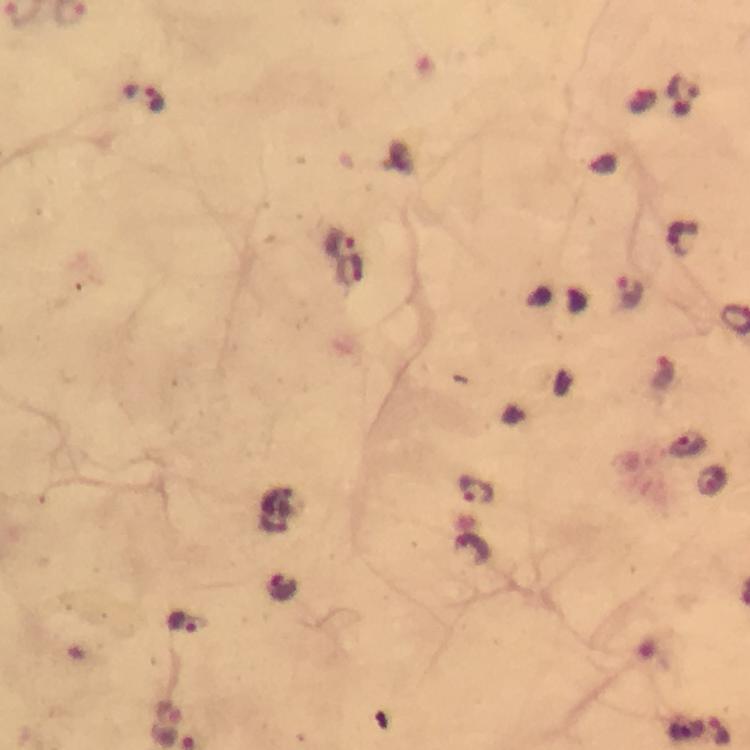 Approximate object centers, in pixels from the top-left corner. Plasmodium parasite locations: (x=141, y=100), (x=681, y=239), (x=341, y=241), (x=630, y=292), (x=664, y=373), (x=689, y=444), (x=712, y=481), (x=476, y=490), (x=475, y=547), (x=281, y=587), (x=183, y=622), (x=718, y=732). 100x magnification. Thick blood smear. Image is 750×750 pixels. Photographed through the microscope with a smartphone camera. A crop from one field of view. From a diagnostic examination for malaria. Immersion oil was used. Giemsa stain.